Give the preparation type.
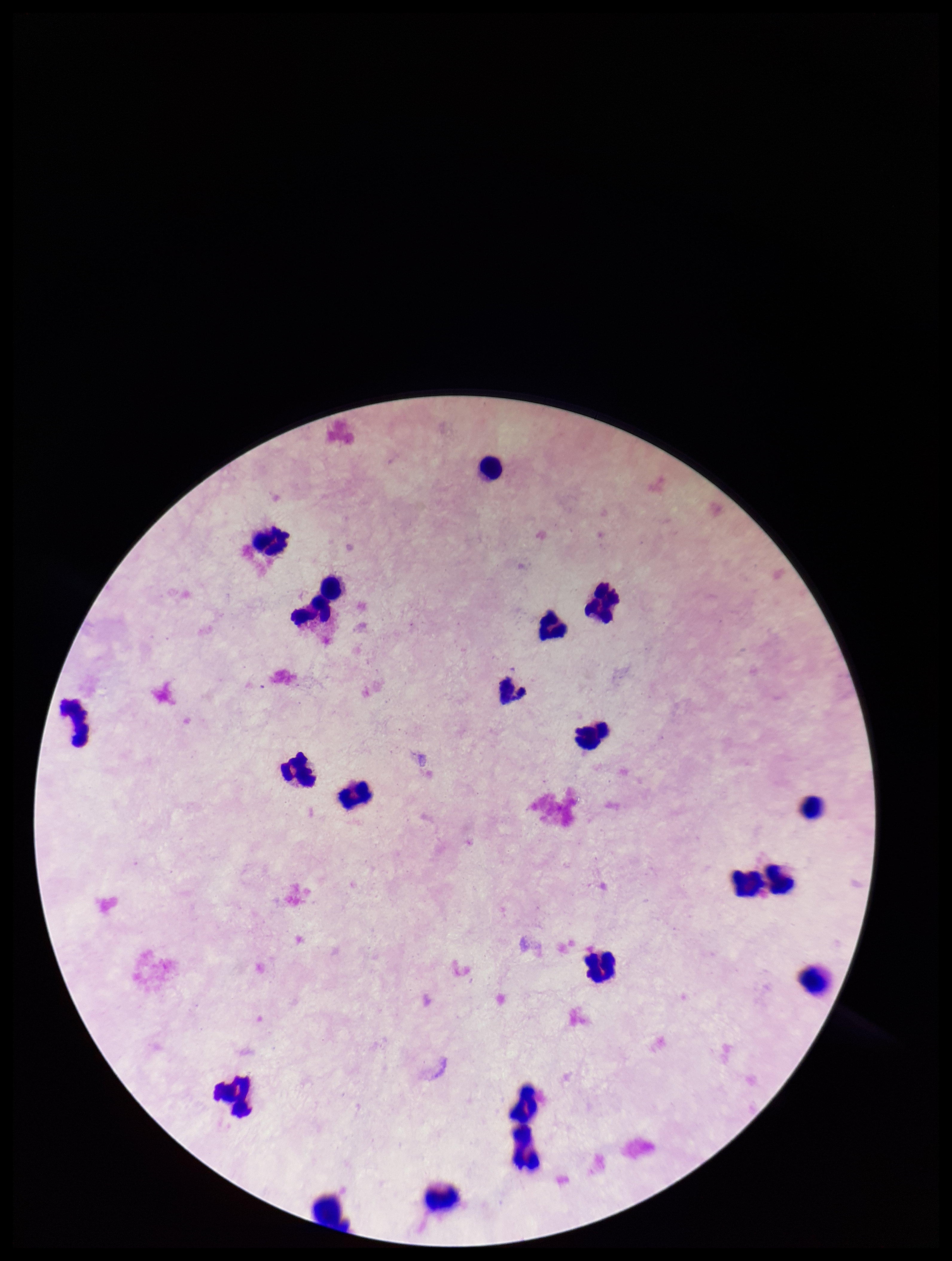
It is a thick blood smear.

Plasmodium parasites = none seen
patient malaria status = negative
leukocyte count = 21
capture = smartphone photograph through the microscope eyepiece
stain = Giemsa
image size = 952×1261 pixels
parasite count = 0
field of view = single